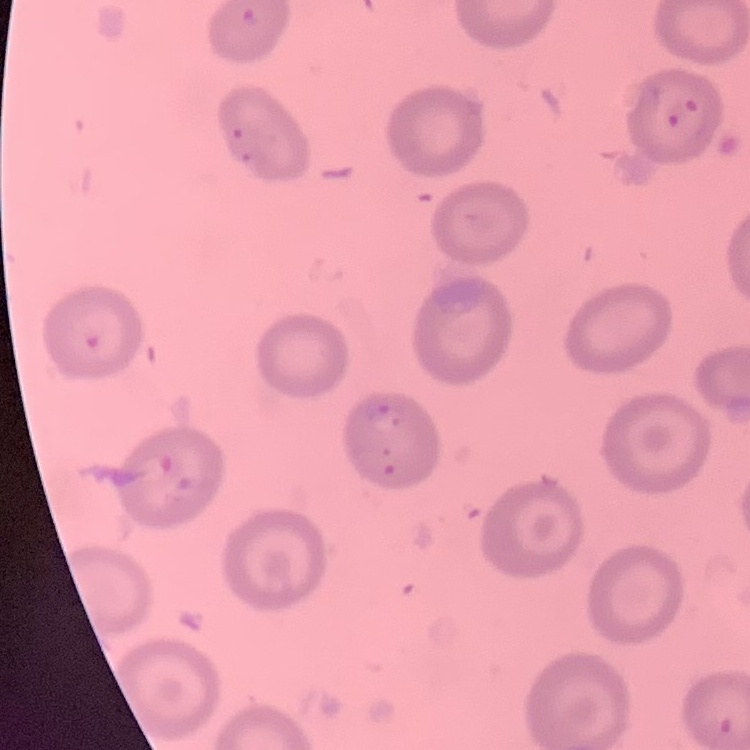

Summary:
  - Red blood cell morphology: no rouleaux formation
  - Image type: square crop of a larger photomicrograph
  - Preparation: thin blood film
  - Stain: Field's or Giemsa